Name the parasite shown.
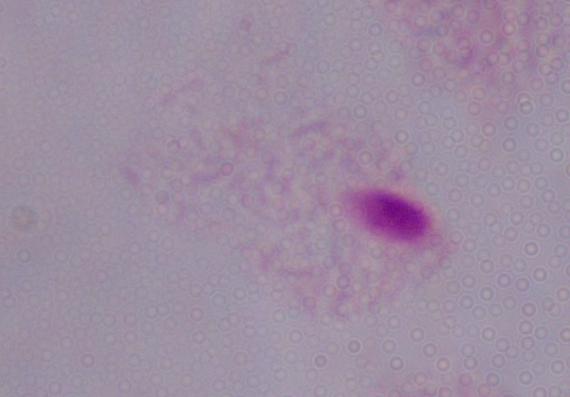

A trichomonad.

Summary:
  - Modality: micrograph
  - Magnification: 1000x